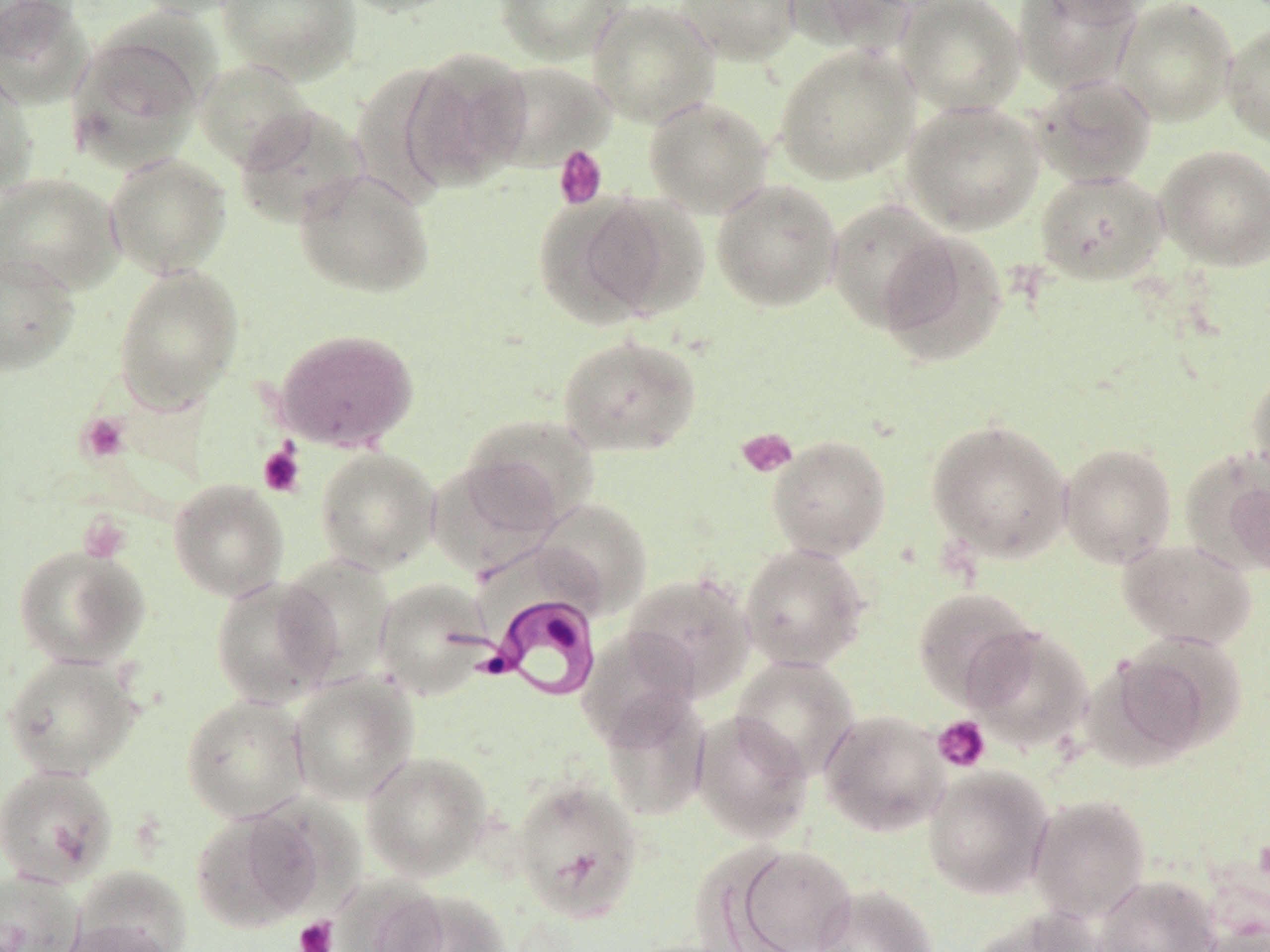

Summary:
  - Coordinate format: approximate bounding boxes as named x1/y1/x2/y2 corners in pixels
  - Trypanosoma brucei locations: (x1=464, y1=590, x2=604, y2=703)
  - Uninfected red blood cell locations: (x1=0, y1=0, x2=92, y2=108), (x1=129, y1=0, x2=257, y2=20), (x1=218, y1=0, x2=361, y2=83), (x1=335, y1=0, x2=466, y2=17), (x1=494, y1=0, x2=631, y2=64), (x1=587, y1=0, x2=720, y2=128), (x1=675, y1=0, x2=802, y2=65), (x1=783, y1=0, x2=918, y2=55), (x1=896, y1=0, x2=1027, y2=116), (x1=1013, y1=0, x2=1143, y2=94), (x1=1113, y1=0, x2=1238, y2=125), (x1=1222, y1=20, x2=1270, y2=147), (x1=69, y1=32, x2=206, y2=168), (x1=774, y1=44, x2=920, y2=185), (x1=403, y1=49, x2=532, y2=191), (x1=193, y1=58, x2=316, y2=170), (x1=482, y1=60, x2=616, y2=172), (x1=0, y1=65, x2=39, y2=197), (x1=1030, y1=74, x2=1157, y2=189), (x1=644, y1=96, x2=773, y2=218), (x1=901, y1=100, x2=1045, y2=235), (x1=234, y1=104, x2=369, y2=228), (x1=1155, y1=144, x2=1270, y2=271), (x1=104, y1=152, x2=232, y2=280), (x1=293, y1=167, x2=436, y2=299), (x1=1034, y1=169, x2=1168, y2=286), (x1=0, y1=172, x2=125, y2=295), (x1=711, y1=179, x2=842, y2=312), (x1=537, y1=193, x2=693, y2=327), (x1=825, y1=198, x2=957, y2=333), (x1=875, y1=230, x2=1009, y2=367), (x1=0, y1=252, x2=80, y2=375), (x1=113, y1=265, x2=244, y2=412), (x1=273, y1=328, x2=420, y2=452), (x1=557, y1=333, x2=702, y2=457), (x1=1246, y1=362, x2=1270, y2=488), (x1=460, y1=412, x2=600, y2=535), (x1=926, y1=418, x2=1072, y2=563), (x1=767, y1=435, x2=892, y2=560), (x1=1058, y1=442, x2=1177, y2=568), (x1=315, y1=448, x2=440, y2=574), (x1=1214, y1=462, x2=1270, y2=580), (x1=168, y1=479, x2=289, y2=601), (x1=533, y1=497, x2=653, y2=618), (x1=1116, y1=539, x2=1257, y2=649), (x1=739, y1=542, x2=870, y2=671), (x1=13, y1=544, x2=150, y2=668), (x1=278, y1=555, x2=396, y2=684), (x1=622, y1=573, x2=755, y2=700), (x1=210, y1=575, x2=342, y2=708), (x1=374, y1=578, x2=495, y2=699), (x1=912, y1=587, x2=1039, y2=707), (x1=963, y1=624, x2=1093, y2=752), (x1=577, y1=626, x2=701, y2=748), (x1=1103, y1=636, x2=1242, y2=762), (x1=1, y1=652, x2=142, y2=780), (x1=730, y1=655, x2=860, y2=780), (x1=289, y1=673, x2=419, y2=805), (x1=600, y1=691, x2=711, y2=820), (x1=181, y1=694, x2=310, y2=822), (x1=818, y1=709, x2=950, y2=837), (x1=691, y1=710, x2=813, y2=842), (x1=361, y1=750, x2=493, y2=882), (x1=0, y1=764, x2=118, y2=888), (x1=922, y1=765, x2=1054, y2=900), (x1=510, y1=775, x2=644, y2=922), (x1=1027, y1=794, x2=1151, y2=923), (x1=191, y1=807, x2=326, y2=932), (x1=730, y1=844, x2=858, y2=952), (x1=70, y1=867, x2=191, y2=951), (x1=0, y1=870, x2=84, y2=952), (x1=1095, y1=874, x2=1220, y2=952), (x1=329, y1=876, x2=450, y2=952), (x1=812, y1=884, x2=938, y2=952), (x1=385, y1=890, x2=511, y2=952), (x1=970, y1=907, x2=1105, y2=952), (x1=58, y1=918, x2=179, y2=952), (x1=1193, y1=921, x2=1270, y2=952)
  - Platelet locations: (x1=553, y1=145, x2=607, y2=210), (x1=76, y1=412, x2=131, y2=464), (x1=736, y1=427, x2=798, y2=478), (x1=258, y1=444, x2=305, y2=497), (x1=78, y1=512, x2=132, y2=563), (x1=932, y1=715, x2=991, y2=773), (x1=294, y1=917, x2=338, y2=952)
  - Slide-level diagnosis: Trypanosoma brucei
  - Field of view: single
  - Magnification: 1000x
  - Image size: 1270×952 pixels
  - Preparation: thin blood film
  - Modality: light microscopy
  - Stain: May-Grünwald-Giemsa